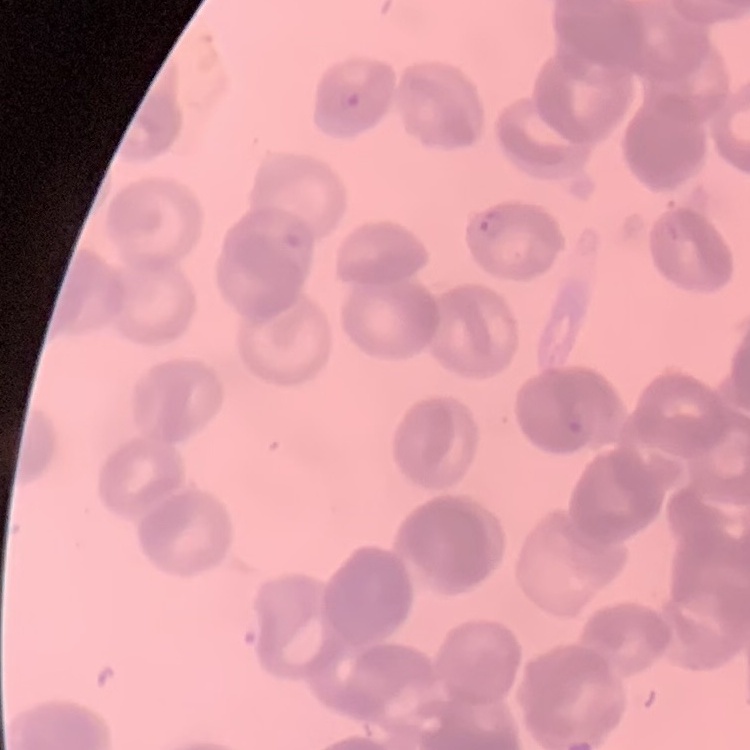 The erythrocytes exhibit rouleaux formation. Square crop of a larger photomicrograph. Field's or Giemsa stain. Thin peripheral smear.